Point out each Plasmodium parasite.
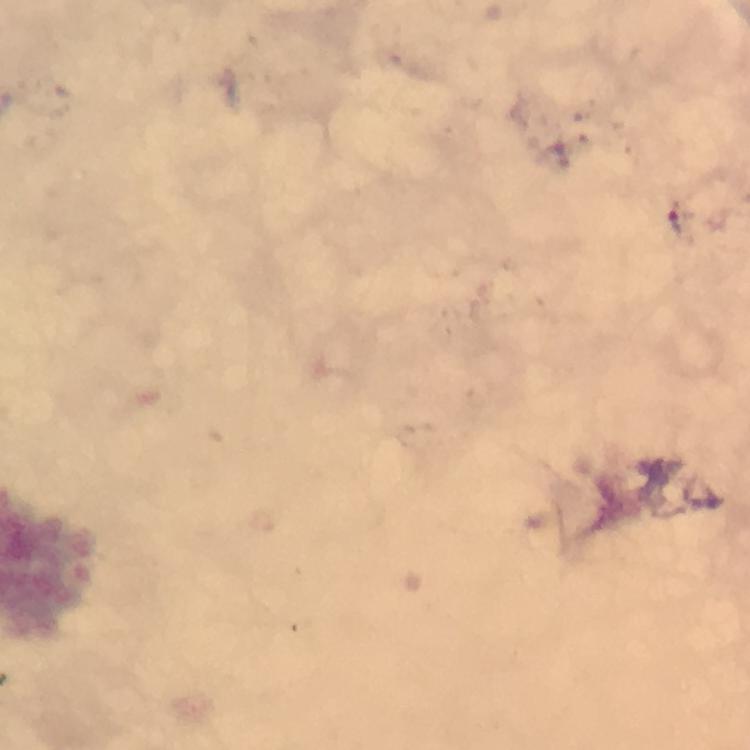
Approximate centers as (x, y) in pixels.
Plasmodium parasites: (679, 222).

Thick smear. Cropped region of a single field of view. Immersion oil applied. Smartphone photograph taken through a microscope. Giemsa-stained preparation. At 100x magnification. Image is 750×750 pixels. From a malaria diagnostic workup.